Name the cell type shown.
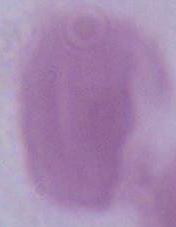
An erythrocyte.

Summary:
  - Modality: micrograph
  - Magnification: 1000x